Identify the parasite.
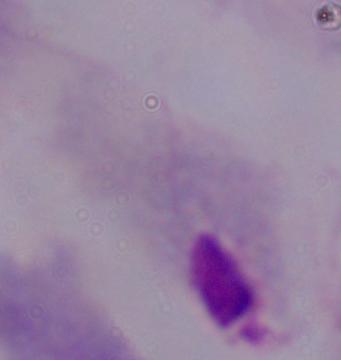

This is a trichomonad.

Summary:
  - Modality: micrograph
  - Magnification: 1000x